Name the parasite shown.
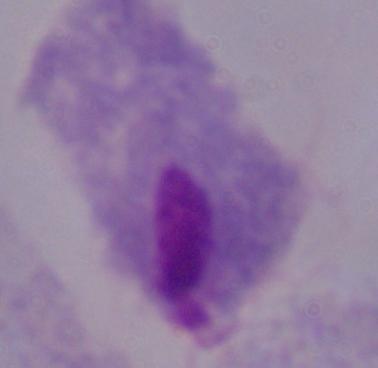
A trichomonad.

magnification = 1000x
modality = photomicrograph